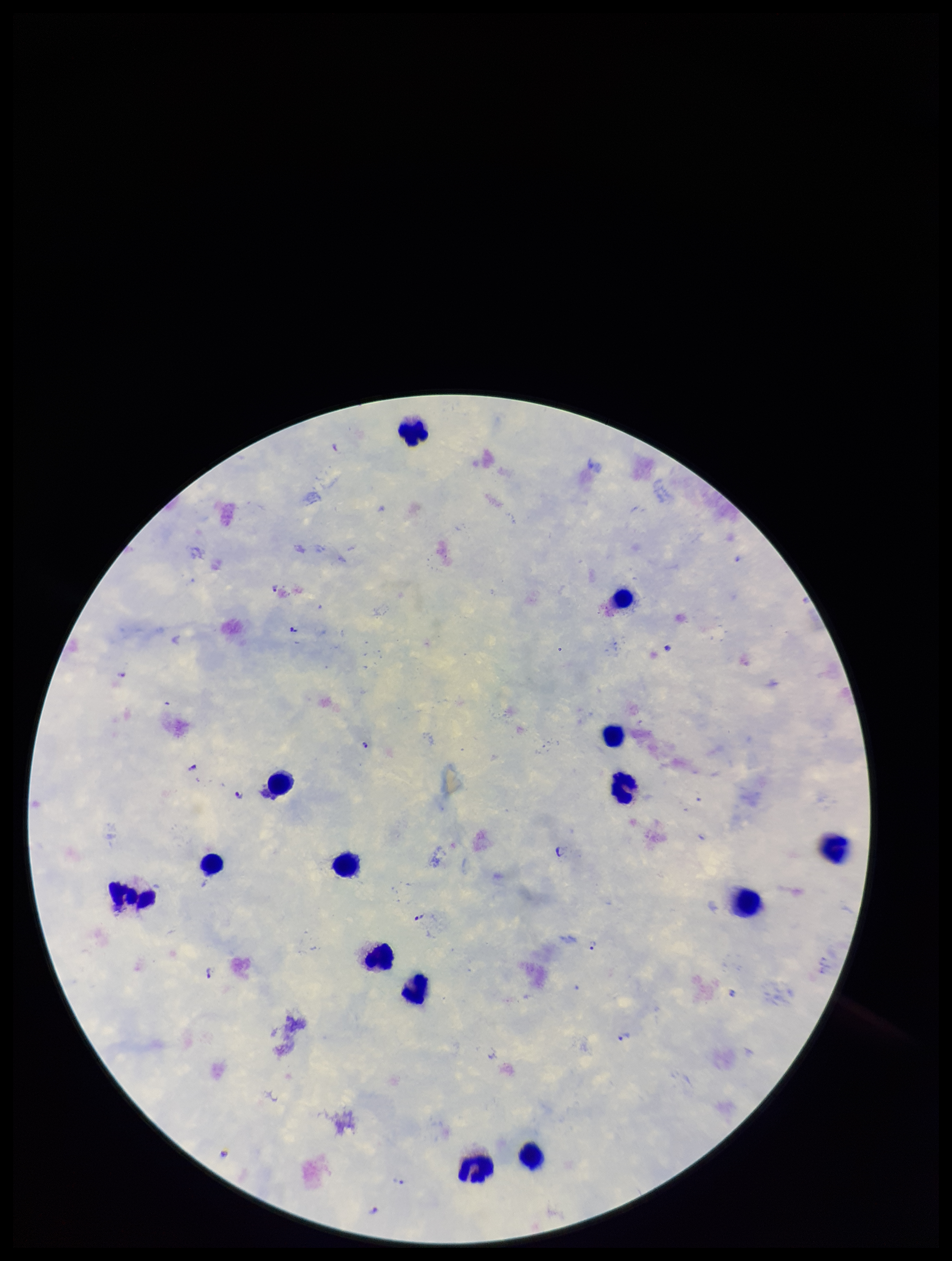
Leukocyte count: 14. Patient malaria status: infected. Parasite count: 11. Photographed through the microscope eyepiece with a smartphone camera. Image is 952×1261 pixels. Plasmodium parasites: detected. Single field of view. Giemsa stain. Species reported for this patient: Plasmodium falciparum. Preparation: thick blood smear.